State the preparation type.
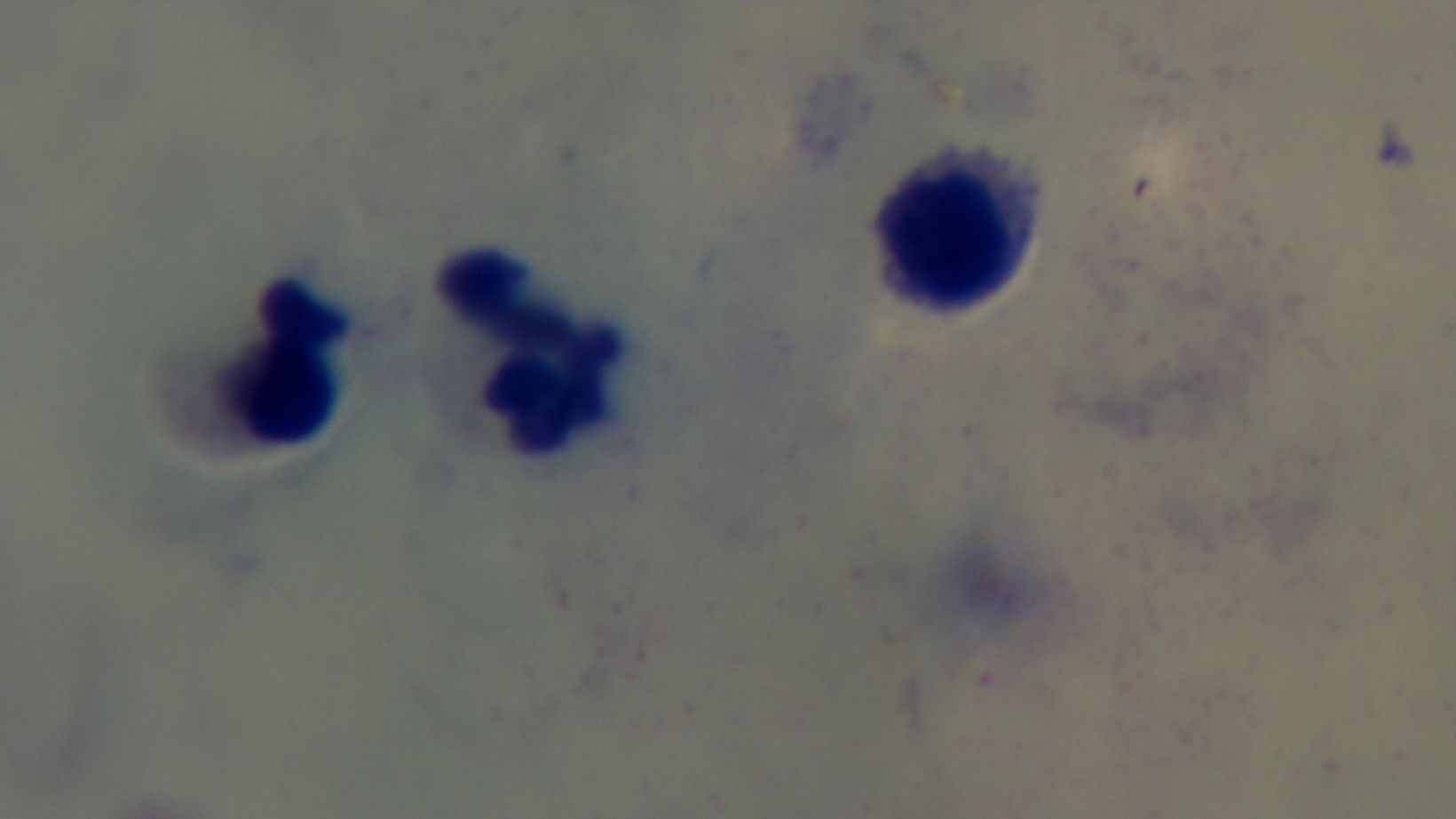
Thick.

Summary:
  - Capture: mounted 4K digital camera
  - Field of view: one from the slide
  - Stain: Giemsa
  - Modality: light microscopy
  - Objective: 100x oil immersion
  - Malaria status: uninfected